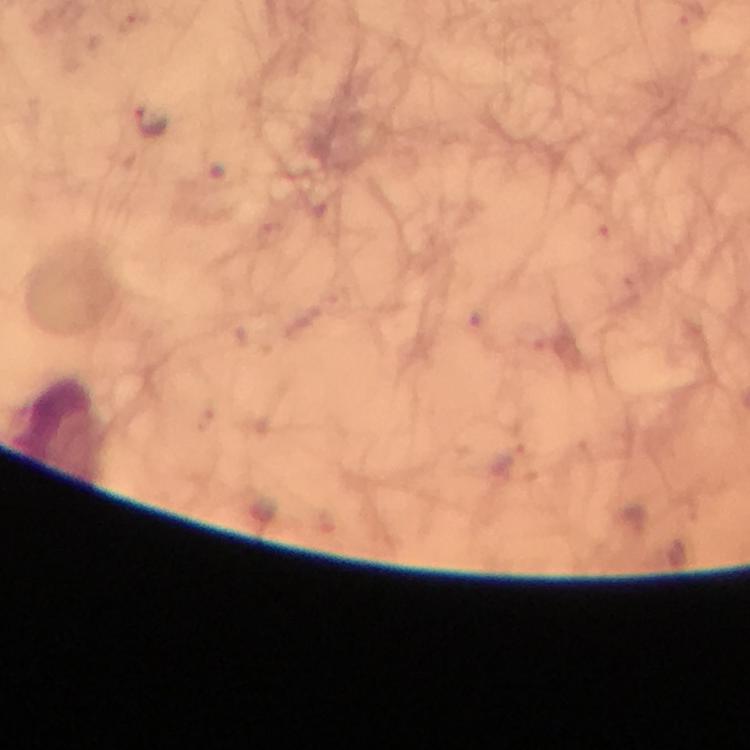

capture: smartphone camera through the microscope
immersion_oil: applied
image_size: 750×750 pixels
context: from a malaria diagnostic workup
stain: Giemsa
preparation: thick smear
plasmodium_parasite_locations: 'approximate object centers, in pixels from the top-left corner: (x=152, y=120)'
cropped_from: a single field of view
magnification: 100x